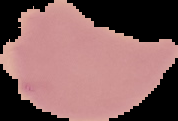 From a thin blood smear. Image is 178×121 pixels. The area outside the segmented cell region is set to black. Malaria status: uninfected.